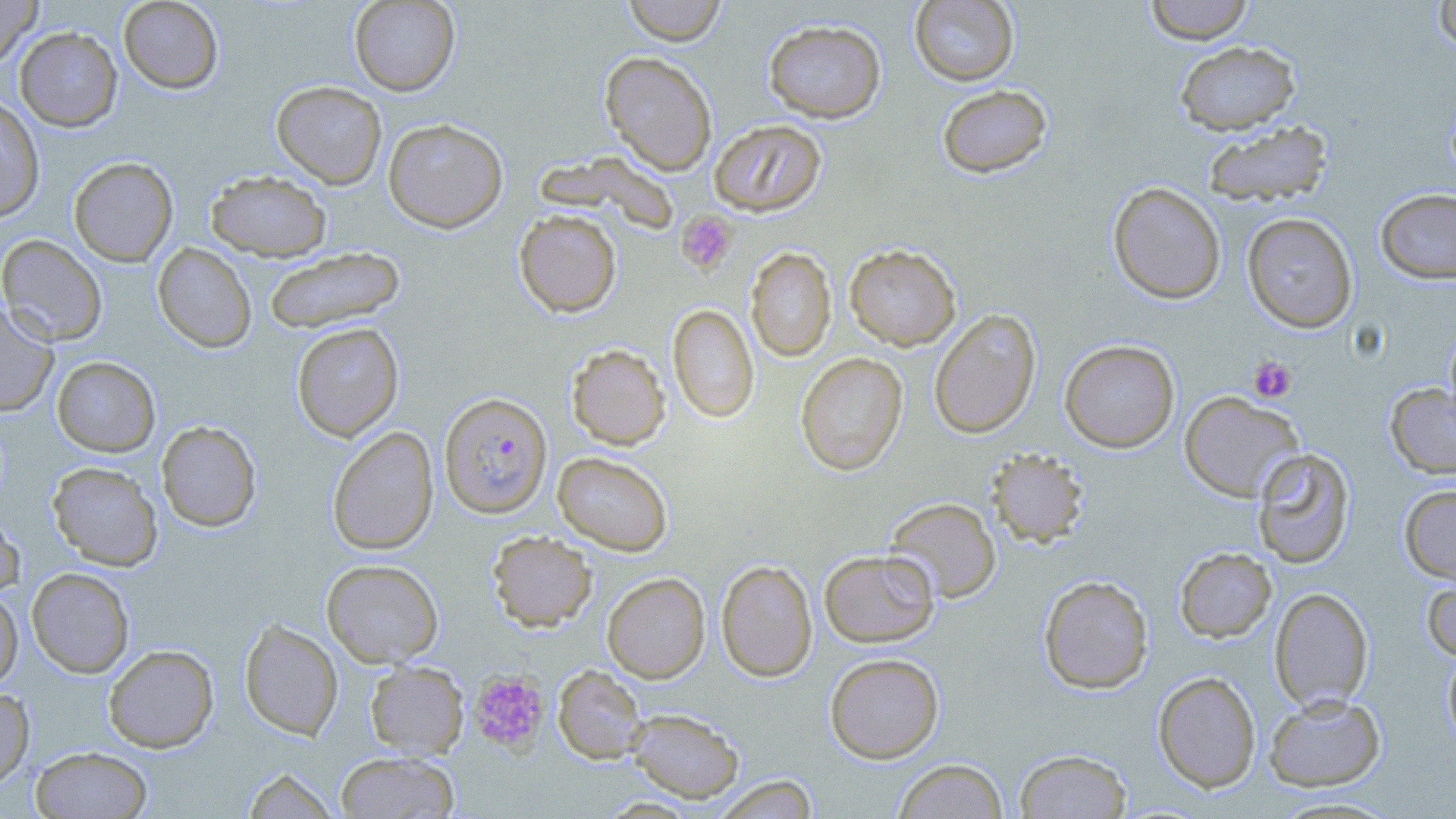

slide-level diagnosis = Plasmodium falciparum
uninfected red blood cell locations = approximate bounding boxes as (x1,y1)-(x2,y2) corner pairs in pixels: (0,0)-(42,71), (118,0)-(224,94), (348,0)-(460,96), (622,0)-(727,46), (909,0)-(1019,86), (1143,0)-(1255,44), (1432,0)-(1456,54), (763,19)-(886,123), (14,27)-(122,131), (1174,40)-(1300,135), (600,51)-(717,175), (271,80)-(387,189), (936,84)-(1052,178), (0,96)-(45,223), (383,118)-(509,233), (708,119)-(827,217), (1201,120)-(1334,208), (538,150)-(679,236), (68,157)-(178,266), (206,170)-(332,261), (1108,181)-(1226,304), (1375,188)-(1456,284), (514,209)-(622,318), (1242,212)-(1358,333), (0,234)-(107,346), (152,243)-(257,353), (844,244)-(961,351), (263,247)-(406,335), (745,247)-(837,362), (0,303)-(58,417), (667,303)-(759,423), (929,309)-(1041,440), (291,322)-(405,441), (1443,323)-(1456,434), (1059,339)-(1180,453), (566,344)-(670,450), (795,352)-(908,476), (52,356)-(161,457), (1385,383)-(1456,479), (1179,391)-(1304,502), (156,420)-(262,532), (327,426)-(439,555), (1252,447)-(1355,569), (986,449)-(1089,549), (552,451)-(673,556), (47,461)-(163,571), (1399,484)-(1456,585), (885,497)-(1001,603), (0,511)-(24,599), (487,531)-(597,631), (1174,546)-(1277,643), (819,549)-(939,647), (321,559)-(444,667), (716,559)-(817,682), (27,567)-(135,678), (1421,568)-(1456,664), (602,572)-(711,683), (1038,574)-(1154,694), (1269,586)-(1374,712), (0,587)-(23,691), (239,618)-(343,740), (103,644)-(219,752), (1442,644)-(1456,754), (825,653)-(944,763), (365,660)-(469,759), (553,665)-(649,765), (1152,670)-(1261,793), (0,687)-(35,789), (1264,693)-(1385,792), (625,708)-(745,803), (30,745)-(153,818), (1014,749)-(1132,818), (334,751)-(459,819), (892,758)-(1009,818), (242,767)-(339,818), (711,775)-(819,818), (1268,795)-(1405,818)
platelet locations = approximate bounding boxes as (x1,y1)-(x2,y2) corner pairs in pixels: (676,210)-(738,275), (1248,357)-(1296,403), (468,670)-(550,754)
field of view = one of a larger specimen
modality = light microscopy
preparation = thin blood smear
magnification = 1000x
stain = May-Grünwald-Giemsa
Plasmodium falciparum-infected red blood cell locations = approximate bounding boxes as (x1,y1)-(x2,y2) corner pairs in pixels: (439,392)-(553,518)
image size = 1456×819 pixels